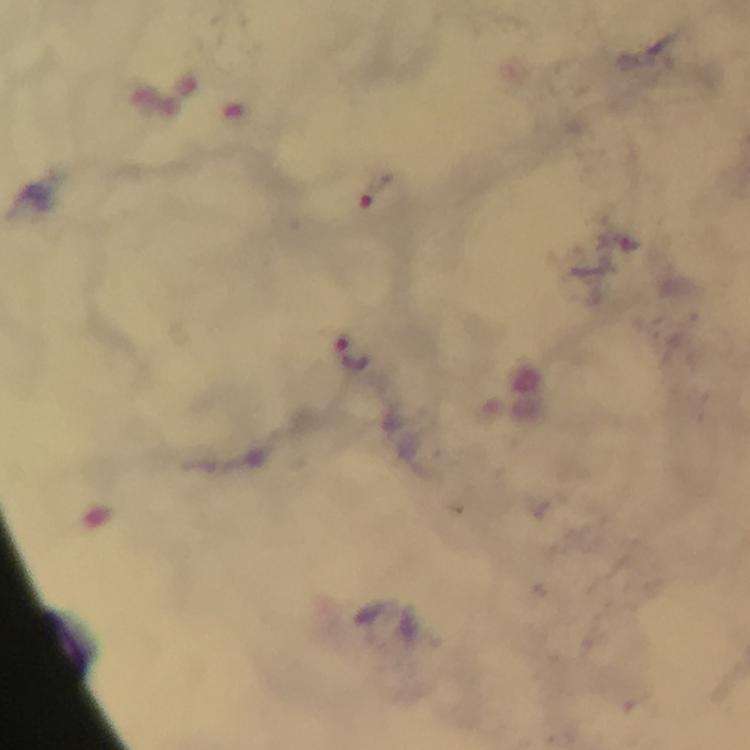

Approximate centers as (x, y) in pixels.
Summary:
  - Plasmodium parasite locations: (373, 193), (354, 350)
  - Cropped from: one field of view
  - Image size: 750×750 pixels
  - Stain: Giemsa
  - Magnification: 100x
  - Capture: smartphone camera through the microscope
  - Context: from a malaria diagnostic workup
  - Preparation: thick blood smear
  - Immersion oil: applied